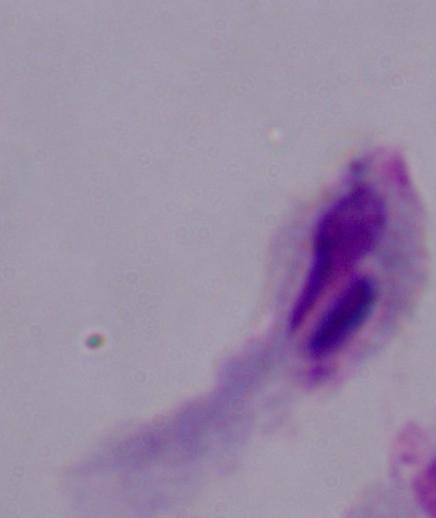 Micrograph. 1000x magnification. A trichomonad is seen.